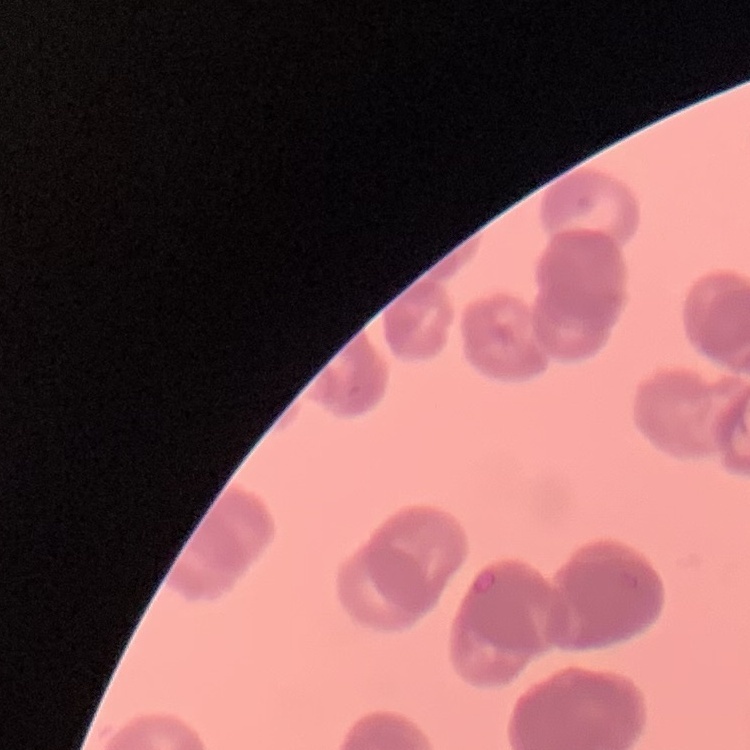

Summary:
  - Erythrocyte morphology: rouleaux formation
  - Image type: one tile cut from a larger photomicrograph
  - Stain: Field's or Giemsa
  - Preparation: thin blood film